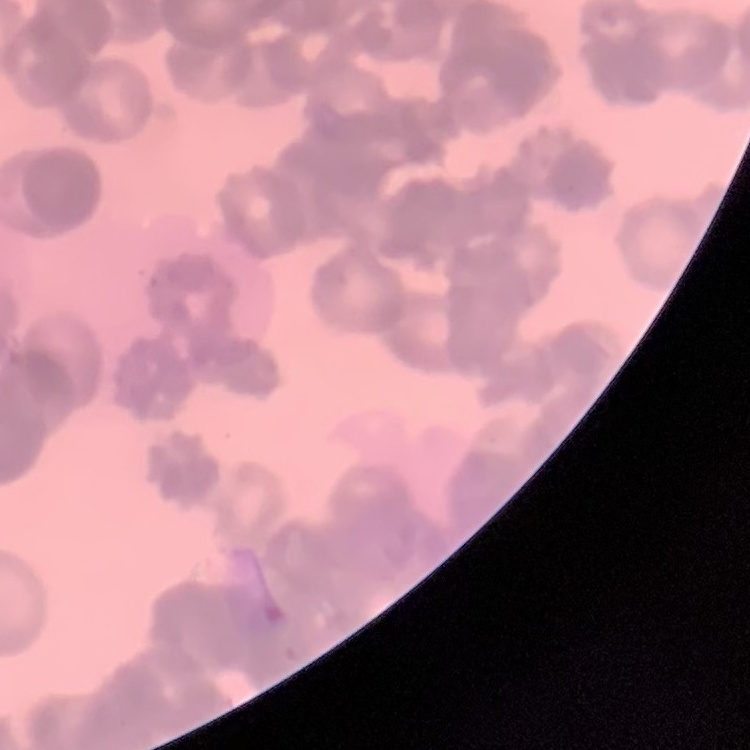

Summary:
  - Erythrocyte morphology: rouleaux formation
  - Image type: one tile cut from a larger photomicrograph
  - Stain: Field's or Giemsa
  - Preparation: thin peripheral smear